Draw a bounding box around every leukocyte (white blood cell).
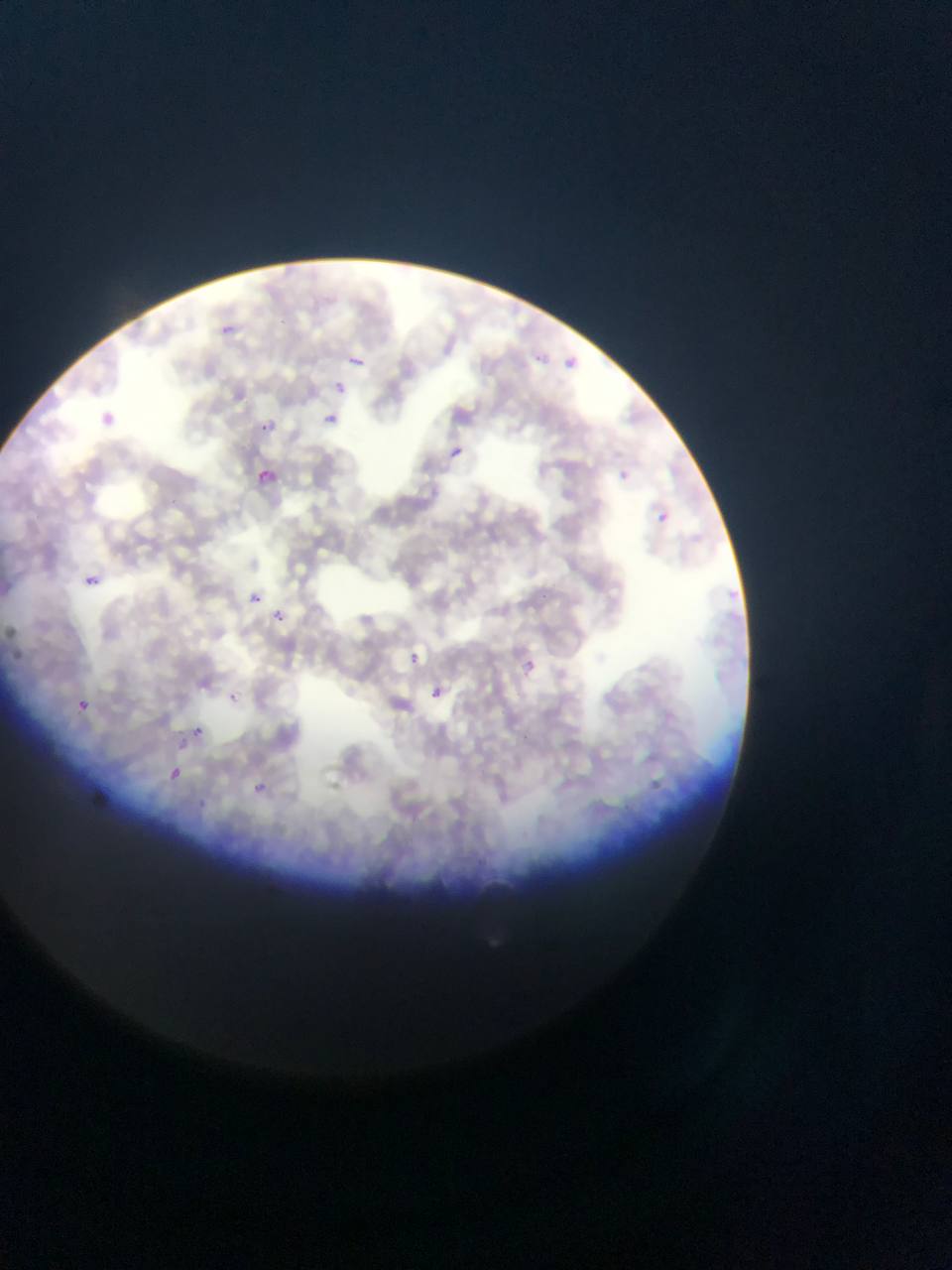

No leukocytes observed.

Approximate bounding boxes as (left, top, right, bottom) in pixels.
Summary:
  - Malaria parasite locations: (208, 310, 248, 340), (529, 344, 551, 366), (566, 352, 589, 369), (347, 355, 366, 365), (328, 378, 351, 400), (99, 402, 117, 424), (329, 409, 342, 428), (254, 417, 278, 437), (448, 444, 465, 460), (252, 465, 279, 491), (612, 465, 633, 487), (650, 506, 675, 529), (84, 574, 100, 589), (245, 588, 266, 609), (266, 605, 292, 629), (401, 648, 425, 670), (517, 658, 538, 677), (422, 682, 450, 708), (74, 698, 91, 714), (187, 722, 207, 743), (164, 764, 185, 784), (246, 777, 272, 800)
  - Artifact (stain precipitate or debris) locations: (647, 773, 673, 796)
  - Capture: mobile-phone photograph through a microscope
  - Field of view: single
  - Country: Ghana
  - Preparation: thin blood smear
  - Image size: 952×1270 pixels